Locate every blood parasite and identify its species.
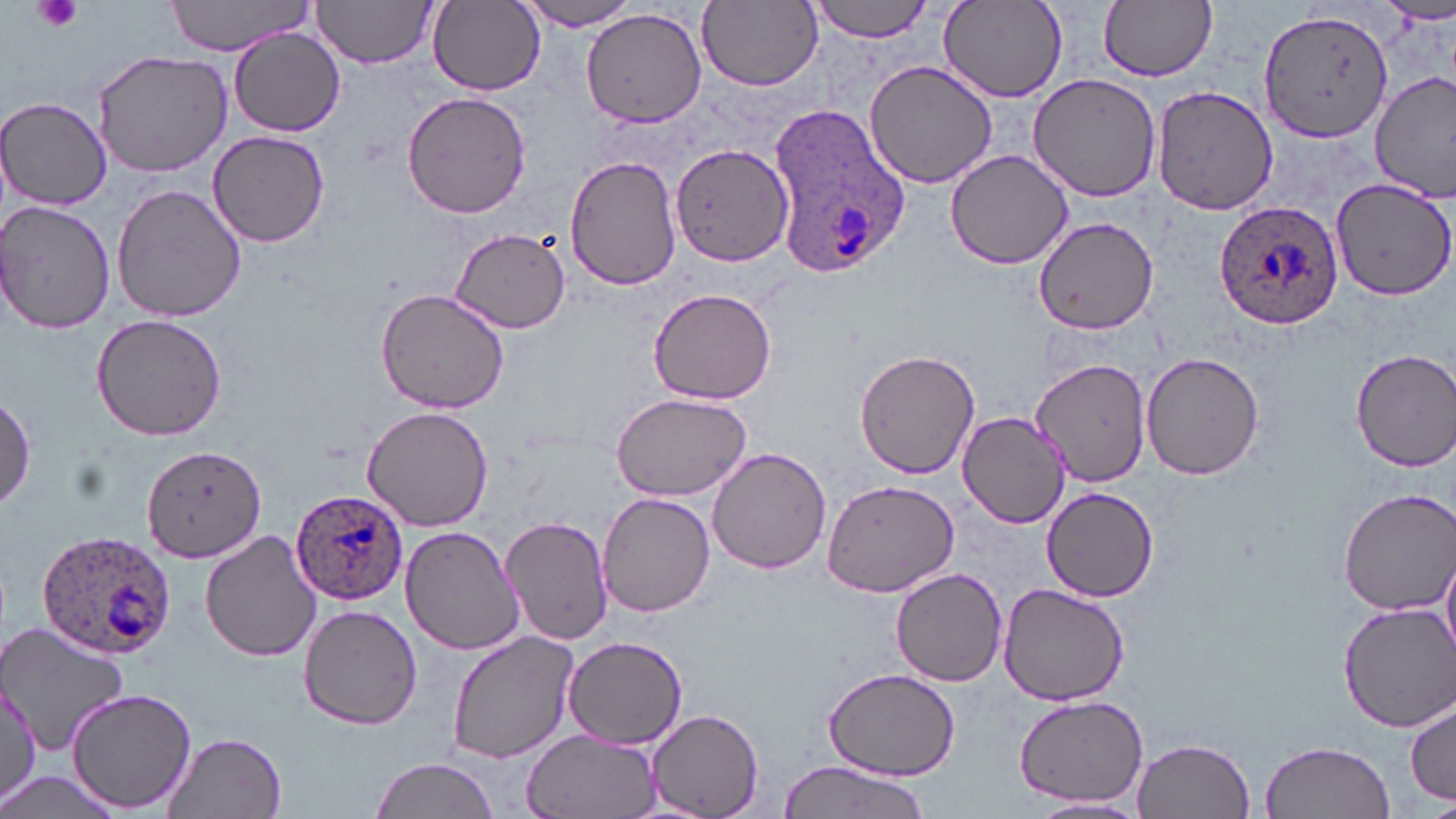

Approximate bounding boxes as [x1, y1, x2, y2] in pixels.
Plasmodium ovale-infected red blood cells: [768, 106, 913, 281], [1214, 198, 1345, 329], [290, 487, 409, 604], [35, 528, 176, 658].
No Plasmodium falciparum, Plasmodium malariae, Plasmodium vivax, Babesia divergens, or Trypanosoma brucei observed.

Uninfected red blood cell locations: [162, 0, 313, 56], [697, 0, 823, 90], [804, 0, 941, 42], [939, 0, 1069, 101], [313, 1, 439, 70], [429, 1, 544, 94], [1098, 1, 1215, 81], [513, 2, 646, 30], [1258, 6, 1395, 141], [581, 7, 705, 130], [228, 29, 346, 137], [91, 49, 234, 177], [864, 60, 998, 190], [1028, 74, 1163, 202], [1371, 74, 1454, 202], [1151, 82, 1278, 214], [402, 91, 530, 218], [1, 97, 111, 209], [208, 130, 330, 245], [670, 140, 793, 267], [945, 149, 1076, 271], [565, 155, 682, 290], [1330, 174, 1456, 300], [110, 183, 248, 323], [1, 199, 116, 335], [1032, 215, 1160, 335], [449, 228, 573, 332], [375, 287, 511, 415], [647, 287, 778, 405], [89, 314, 227, 441], [855, 348, 981, 480], [1351, 348, 1456, 470], [1140, 350, 1267, 480], [1028, 356, 1151, 487], [0, 393, 35, 516], [608, 393, 753, 499], [362, 406, 492, 532], [958, 412, 1070, 528], [141, 447, 264, 564], [707, 447, 832, 574], [822, 479, 959, 598], [1042, 486, 1160, 603], [1334, 486, 1456, 614], [598, 493, 715, 619], [501, 514, 615, 644], [399, 527, 523, 654], [201, 530, 322, 663], [1440, 548, 1456, 660], [890, 569, 1007, 687], [996, 581, 1132, 706], [1334, 601, 1456, 732], [298, 604, 422, 730], [0, 620, 129, 756], [447, 632, 578, 765], [563, 634, 689, 750], [827, 667, 960, 779], [0, 684, 38, 808], [66, 686, 198, 812], [1014, 693, 1151, 807], [1406, 699, 1456, 804], [646, 708, 764, 819], [520, 730, 662, 819], [159, 732, 289, 817], [1133, 736, 1257, 819], [1261, 739, 1394, 819], [369, 755, 501, 819], [778, 760, 933, 819], [0, 765, 119, 819], [1026, 796, 1149, 817]. Platelet locations: [34, 0, 83, 34]. Slide-level diagnosis: Plasmodium ovale. One field of a larger specimen. Image is 1456×819 pixels. Thin blood film. Optical microscopy. 1000x magnification. May-Grünwald-Giemsa stain.